Name the cell type shown.
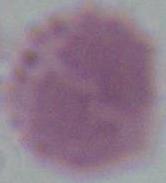
This is an erythrocyte.

modality = micrograph
magnification = 1000x